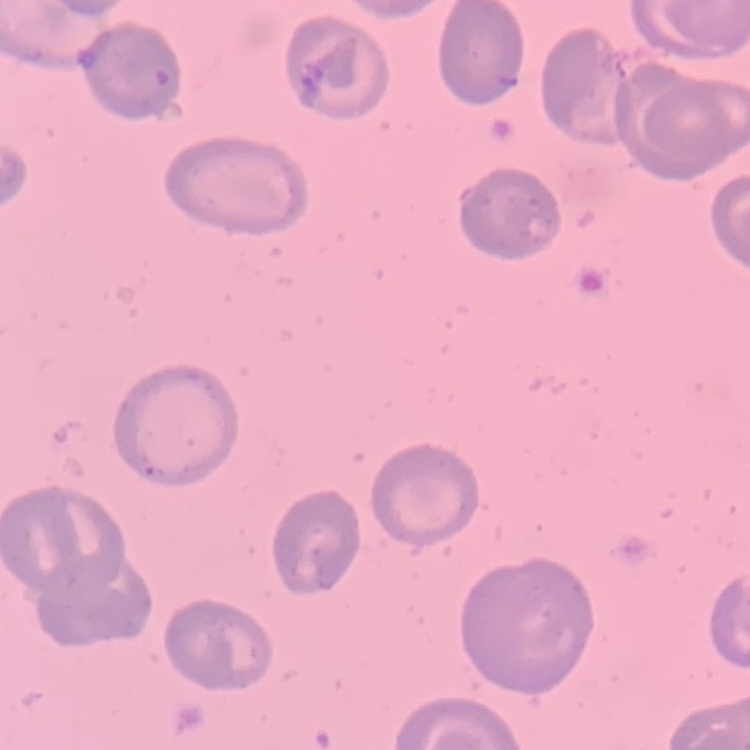
The erythrocytes show no rouleaux formation. Stained with either Field's or Giemsa. Square crop of a larger photomicrograph. Thin peripheral smear.